Comment on the morphology of the erythrocytes.
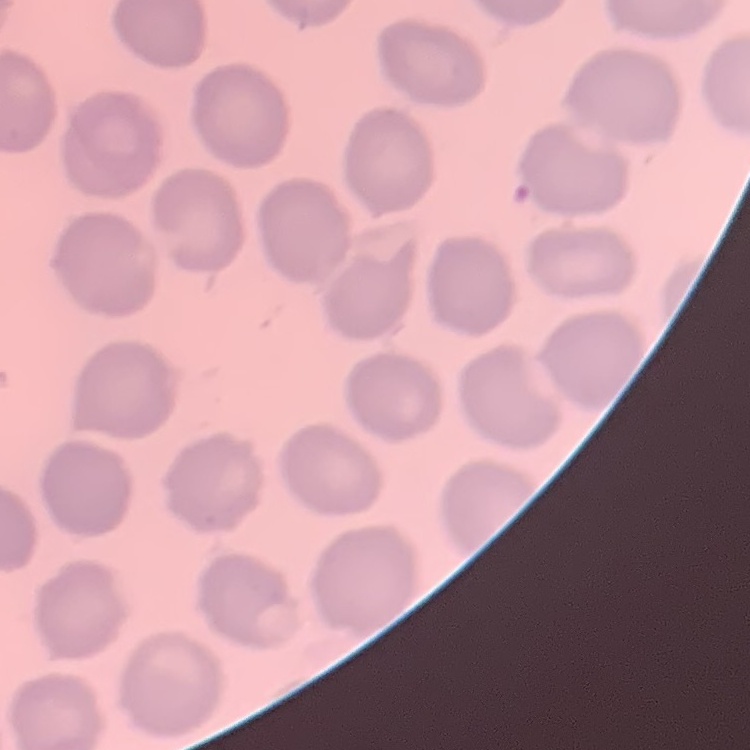

No rouleaux formation.

Field's or Giemsa stain. Thin blood smear. Square crop of a larger photomicrograph.